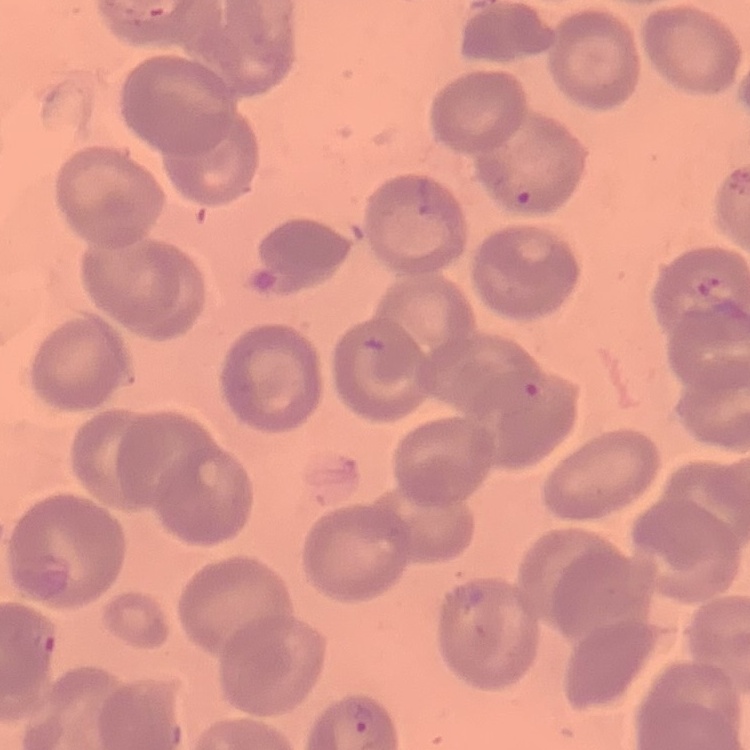
The red blood cells exhibit no rouleaux formation. Thin blood film. Field's or Giemsa stain. Square crop of a larger photomicrograph.